Assess this cell for malaria.
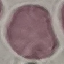

It is uninfected.

image_type: cell patch, automatically extracted from a larger field of view and resized to 64 × 64 pixels
stain: Giemsa
preparation: thin smear
capture: smartphone through the microscope eyepiece